Describe the morphology of the red blood cells.
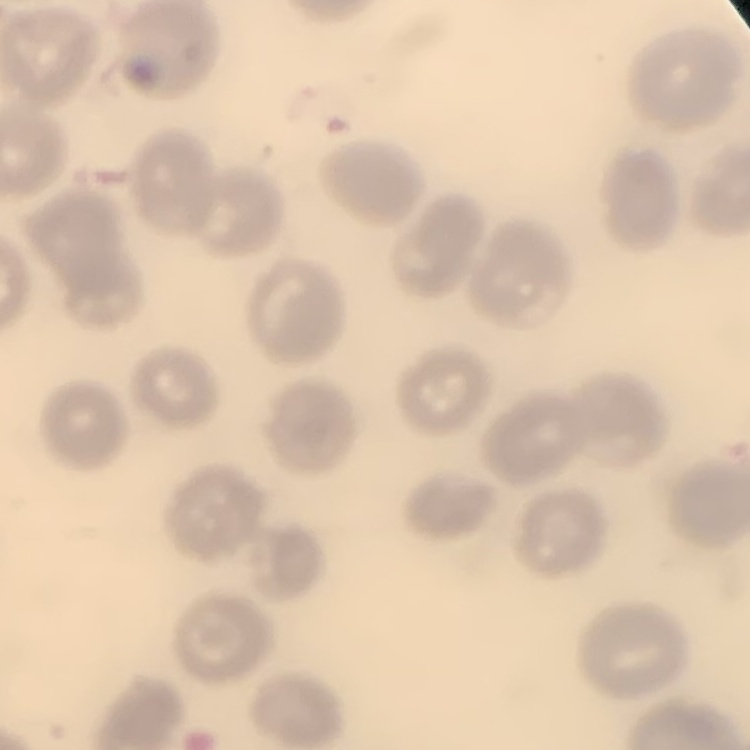

No rouleaux formation.

Field's or Giemsa stain. Thin blood film. One tile cut from a larger photomicrograph.